Assess this cell for malaria.
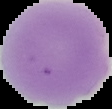
Uninfected.

Summary:
  - Preparation: thin blood film
  - Image size: 112×109 pixels
  - Image type: cell region segmented out of the field of view; surrounding area masked to black